State the blood parasite species.
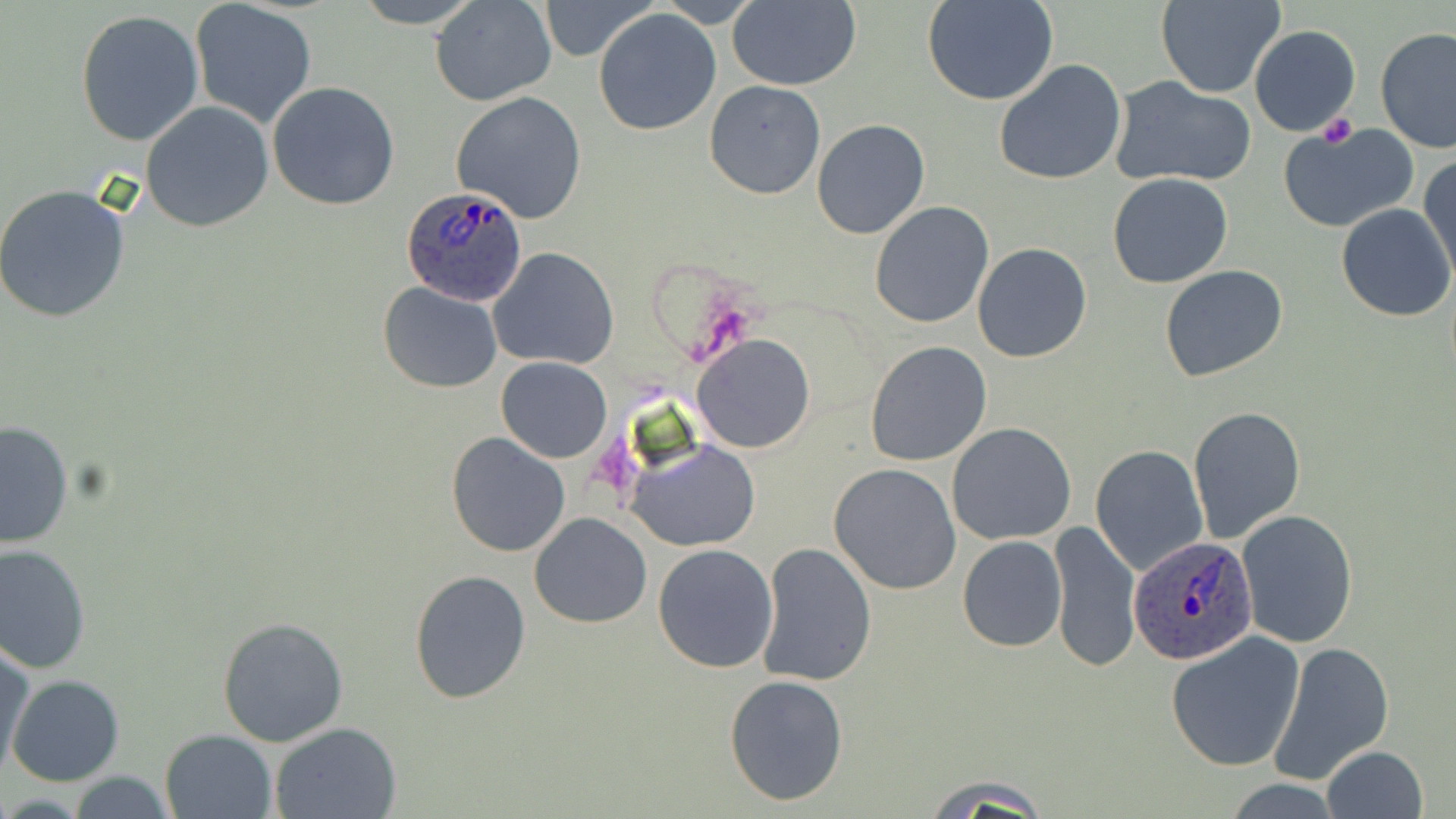

Plasmodium ovale.

Approximate bounding boxes as [x1, y1, x2, y2] in pixels. Platelet locations: [1317, 115, 1357, 148]. Plasmodium ovale-infected red blood cell locations: [398, 186, 527, 308], [1128, 535, 1258, 666]. Uninfected red blood cell locations: [350, 0, 484, 28], [656, 0, 761, 27], [726, 0, 860, 90], [924, 0, 1059, 106], [1156, 0, 1284, 98], [188, 1, 318, 129], [430, 1, 557, 106], [541, 2, 652, 61], [592, 8, 722, 136], [75, 9, 205, 147], [1248, 25, 1361, 137], [1374, 27, 1456, 155], [993, 58, 1129, 186], [1110, 76, 1257, 189], [704, 81, 825, 200], [268, 82, 401, 210], [449, 92, 590, 225], [140, 102, 274, 231], [811, 118, 930, 239], [1278, 121, 1419, 234], [1419, 155, 1456, 285], [1108, 174, 1234, 289], [0, 183, 132, 323], [869, 201, 994, 329], [1336, 202, 1455, 322], [971, 243, 1092, 364], [488, 247, 619, 370], [1160, 265, 1289, 384], [378, 281, 503, 393], [693, 334, 816, 454], [865, 340, 993, 467], [495, 356, 613, 464], [1188, 405, 1305, 542], [0, 422, 73, 550], [946, 423, 1077, 546], [444, 432, 571, 558], [628, 440, 761, 552], [1091, 445, 1209, 576], [830, 462, 962, 595], [1237, 509, 1358, 648], [529, 512, 653, 627], [1049, 518, 1142, 674], [957, 536, 1068, 653], [1, 542, 93, 674], [757, 542, 877, 688], [652, 544, 779, 672], [408, 568, 530, 704], [217, 615, 349, 747], [1165, 632, 1305, 772], [1271, 639, 1392, 785], [0, 643, 35, 777], [725, 673, 849, 805], [7, 674, 124, 787], [270, 721, 404, 818], [162, 729, 277, 819], [1320, 746, 1428, 819], [67, 772, 178, 818], [923, 773, 1050, 816]. May-Grünwald-Giemsa stain. Thin blood film. One field of a larger specimen. Optical microscopy. Image is 1456×819 pixels. 1000x magnification.